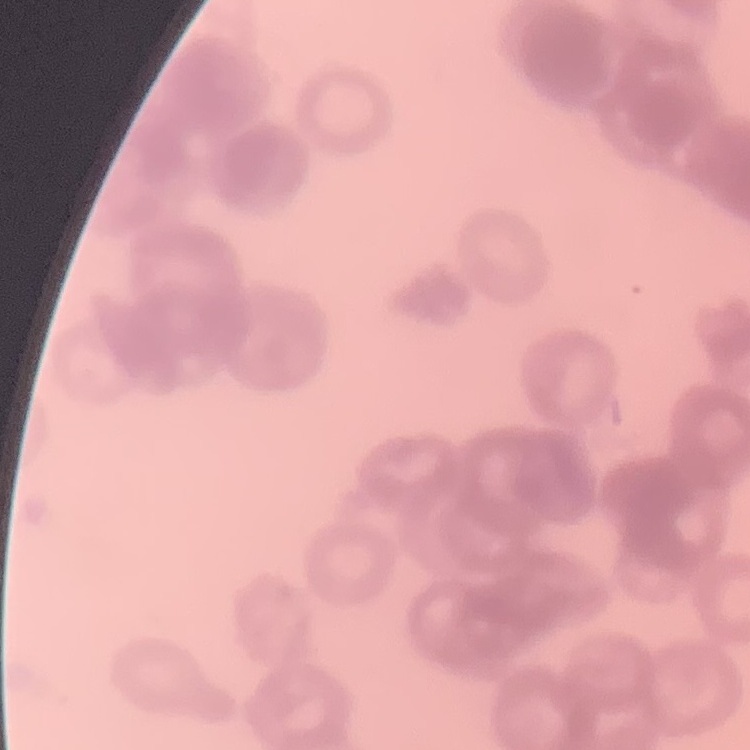

The red blood cells exhibit rouleaux formation. One tile cut from a larger photomicrograph. Thin blood smear. Stained with either Field's or Giemsa.